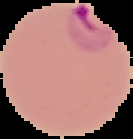

Summary:
  - Malaria status: parasitized
  - Image size: 133×139 pixels
  - Preparation: thin blood film
  - Image type: segmented cell region on a black background